Identify the parasite.
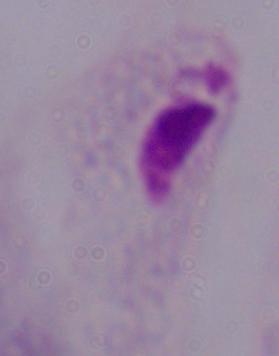
This is a trichomonad.

1000x magnification. Photomicrograph.